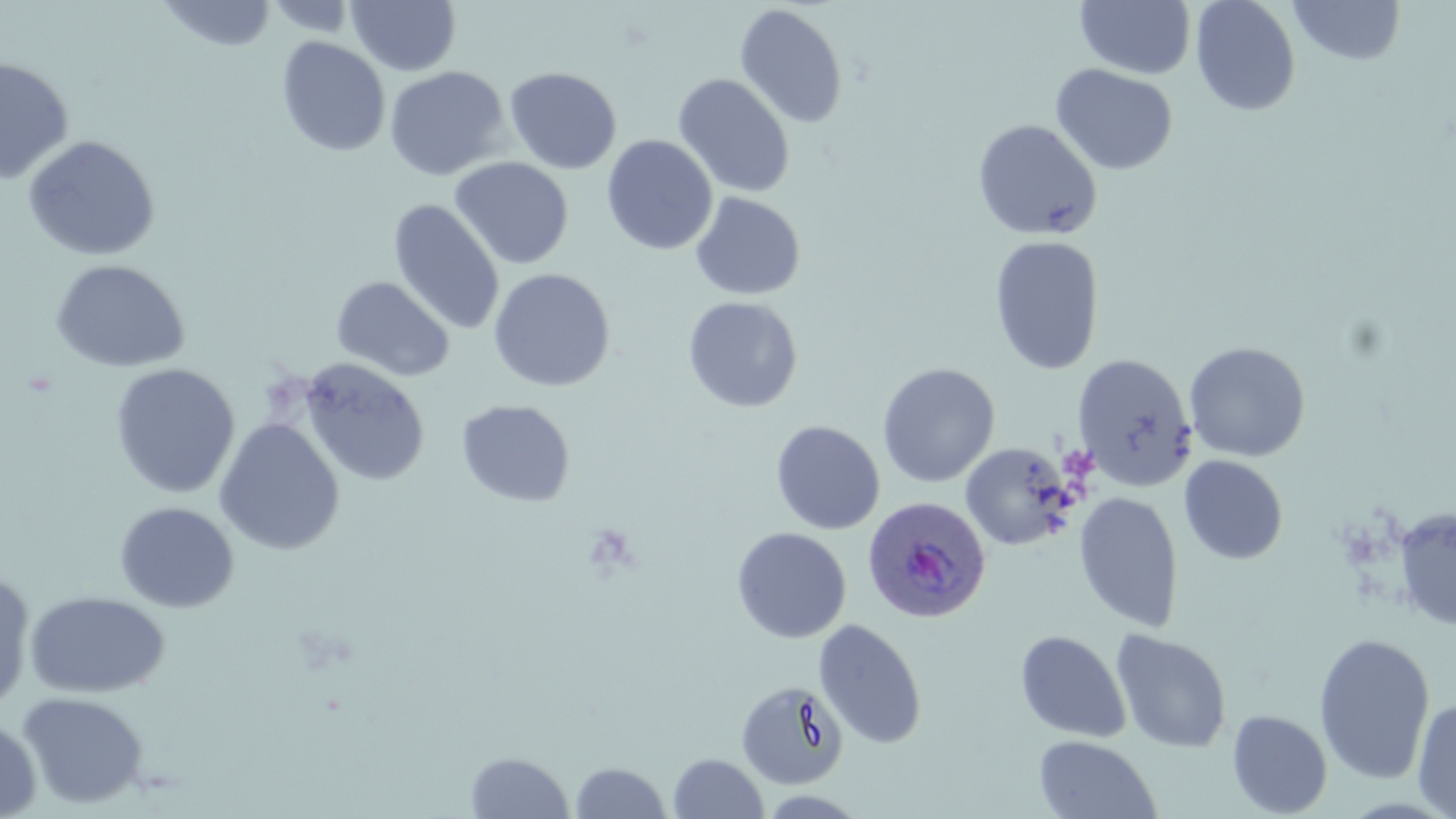

slide-level diagnosis = Plasmodium ovale
uninfected red blood cell locations = approximate bounding boxes as (x1,y1)-(x2,y2) corner pairs in pixels: (157,0)-(277,52), (263,0)-(360,38), (346,0)-(461,76), (1075,0)-(1196,79), (1190,0)-(1301,116), (1288,0)-(1406,65), (733,3)-(848,129), (276,36)-(391,157), (0,57)-(74,184), (1050,64)-(1178,176), (383,66)-(510,181), (503,66)-(622,174), (672,73)-(795,198), (972,119)-(1102,240), (22,135)-(160,261), (601,135)-(719,256), (449,157)-(573,270), (690,191)-(806,301), (387,199)-(505,335), (988,235)-(1105,376), (51,259)-(189,373), (488,268)-(616,392), (330,275)-(455,382), (682,296)-(803,413), (1183,341)-(1311,462), (1072,354)-(1197,491), (297,358)-(430,487), (110,363)-(240,499), (877,363)-(1000,487), (456,399)-(575,507), (214,418)-(345,556), (770,420)-(885,535), (960,442)-(1076,551), (1178,455)-(1288,565), (1073,492)-(1184,632), (114,501)-(239,613), (1391,505)-(1456,632), (731,527)-(852,643), (0,569)-(36,716), (25,591)-(170,698), (812,618)-(927,749), (1110,628)-(1232,753), (1014,629)-(1131,743), (1313,632)-(1436,784), (735,679)-(849,790), (17,691)-(149,809), (1412,697)-(1456,818), (1227,709)-(1332,818), (0,716)-(41,819), (1033,734)-(1161,819), (465,750)-(574,818), (667,752)-(769,818), (569,761)-(672,818), (756,790)-(871,818)
modality = light microscopy
stain = May-Grünwald-Giemsa
preparation = thin blood smear
Plasmodium ovale-infected red blood cell locations = approximate bounding boxes as (x1,y1)-(x2,y2) corner pairs in pixels: (860,496)-(990,625)
magnification = 1000x
field of view = one of a larger specimen
image size = 1456×819 pixels